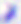
Summary:
  - Modality: photomicrograph
  - Magnification: 400x
  - Identification: Toxoplasma gondii